Identify the parasite.
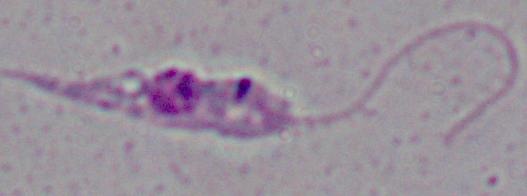
This is Leishmania.

Photomicrograph. 1000x magnification.